Locate every Plasmodium parasite.
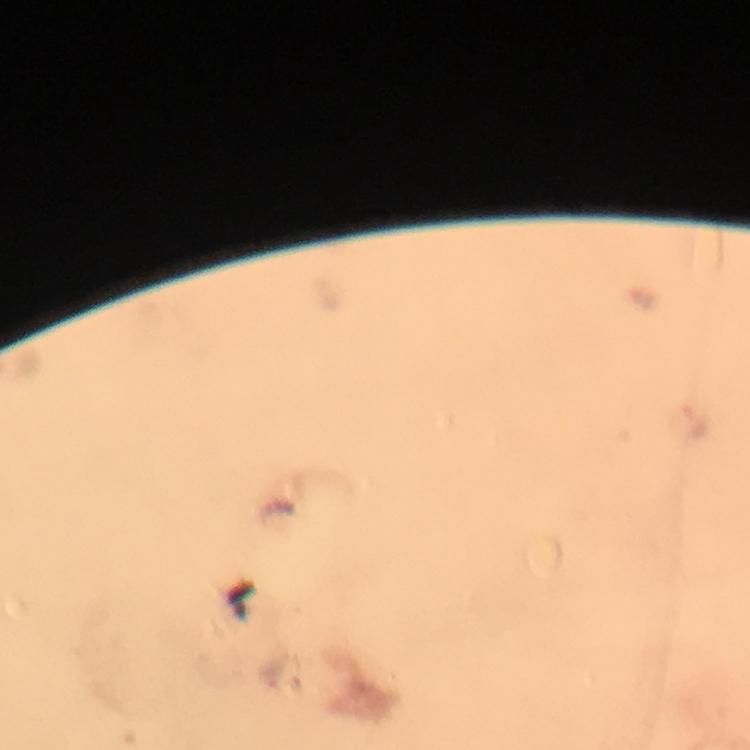

Approximate centers as {x, y} in pixels.
Plasmodium parasites: {695, 425}.

capture: smartphone camera through the microscope
immersion_oil: used
image_size: 750×750 pixels
magnification: 100x
cropped_from: a single field of view
context: from a diagnostic examination for malaria
stain: Giemsa
preparation: thick smear